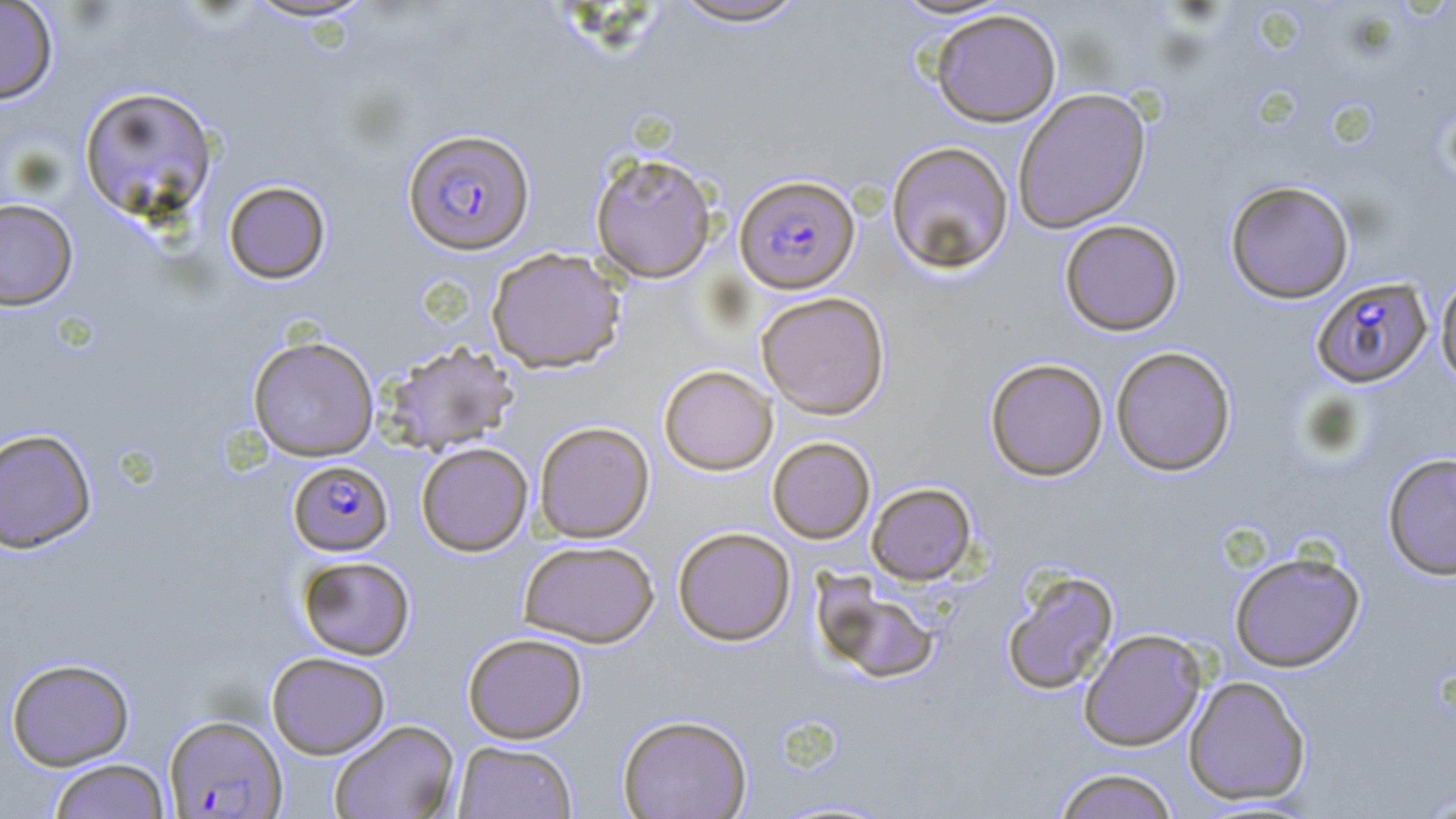
Summary:
  - Coordinate format: approximate bounding boxes as (x1, y1, x2, y2) in pixels
  - Uninfected red blood cell locations: (0, 0, 59, 105), (239, 0, 379, 23), (889, 0, 1016, 21), (668, 1, 811, 28), (930, 9, 1062, 127), (78, 85, 219, 222), (1012, 87, 1152, 233), (885, 141, 1014, 273), (590, 151, 718, 283), (222, 180, 332, 284), (1224, 180, 1355, 304), (0, 198, 79, 311), (1059, 219, 1183, 336), (486, 247, 626, 373), (1435, 269, 1456, 392), (756, 291, 891, 419), (247, 335, 379, 461), (381, 341, 520, 456), (1110, 345, 1237, 476), (985, 358, 1108, 481), (658, 364, 778, 475), (533, 420, 655, 543), (0, 428, 97, 554), (767, 436, 875, 544), (416, 442, 533, 556), (1382, 452, 1456, 581), (866, 482, 977, 585), (672, 526, 796, 645), (518, 539, 659, 648), (1228, 549, 1366, 672), (284, 554, 400, 757), (297, 555, 416, 660), (1001, 568, 1120, 696), (812, 573, 941, 684), (1078, 628, 1207, 751), (462, 632, 588, 743), (266, 651, 390, 759), (6, 657, 135, 770), (1183, 675, 1312, 805), (617, 713, 753, 819), (329, 719, 460, 819), (452, 740, 578, 818), (47, 759, 171, 818), (1051, 768, 1180, 819)
  - Plasmodium falciparum-infected red blood cell locations: (402, 128, 536, 256), (734, 174, 860, 293), (1310, 276, 1433, 388), (288, 460, 393, 556), (163, 714, 288, 817)
  - Slide-level diagnosis: Plasmodium falciparum
  - Field of view: one of a larger specimen
  - Magnification: 1000x
  - Modality: optical microscopy
  - Stain: May-Grünwald-Giemsa
  - Image size: 1456×819 pixels
  - Preparation: thin blood smear